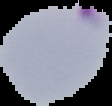

Summary:
  - Image size: 112×106 pixels
  - Preparation: thin blood film
  - Result: Plasmodium parasites detected
  - Image type: cell region segmented out of the field of view; surrounding area masked to black